Classify this cell by malaria status.
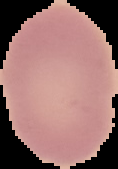
Uninfected.

preparation: thin blood film
image_type: segmented cell region on a black background
image_size: 118×169 pixels